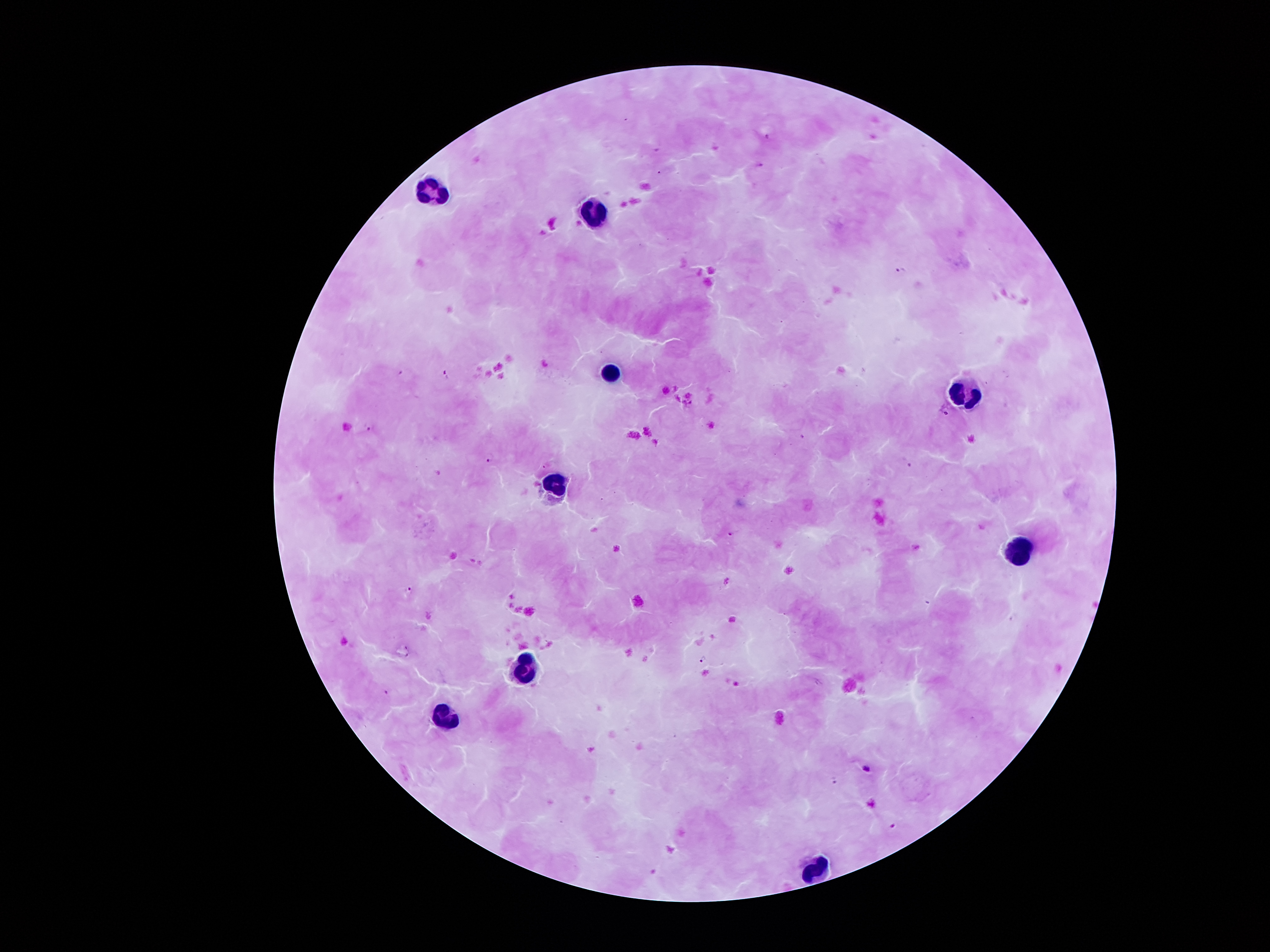
Approximate object centers, in pixels from the top-left corner. Plasmodium parasite locations: (x=768, y=138), (x=759, y=165), (x=901, y=270), (x=401, y=373), (x=448, y=374), (x=370, y=427), (x=491, y=458), (x=909, y=464), (x=546, y=467), (x=733, y=533), (x=409, y=590), (x=703, y=660), (x=387, y=694), (x=866, y=767), (x=834, y=779), (x=896, y=824). Leukocyte locations: (x=430, y=197), (x=592, y=216), (x=608, y=373), (x=967, y=386), (x=553, y=482), (x=1014, y=553), (x=524, y=669), (x=446, y=719), (x=816, y=868). 100x magnification. Photographed through the microscope eyepiece with a smartphone camera. One field from this slide. Image is 1270×952 pixels. Giemsa stain. Patient malaria status: positive for Plasmodium falciparum. Thick blood film.